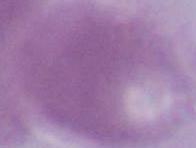
{
  "modality": "micrograph",
  "identification": "red blood cell",
  "magnification": "1000x"
}